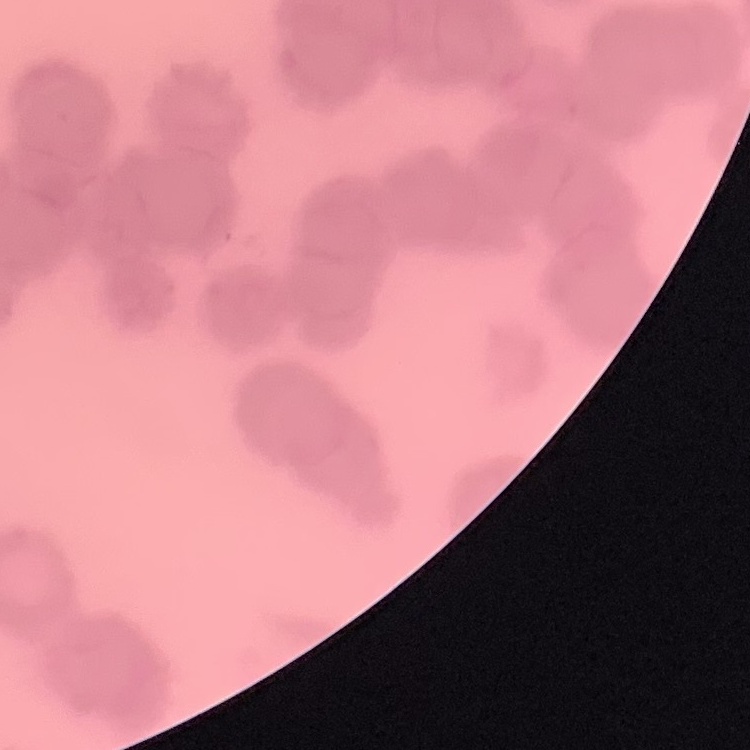

Summary:
  - Erythrocyte morphology: rouleaux formation
  - Preparation: thin blood smear
  - Stain: Field's or Giemsa
  - Image type: square crop of a larger photomicrograph